State which parasite is depicted.
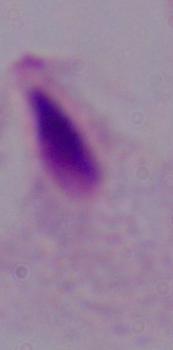
This is a trichomonad.

modality: micrograph
magnification: 1000x